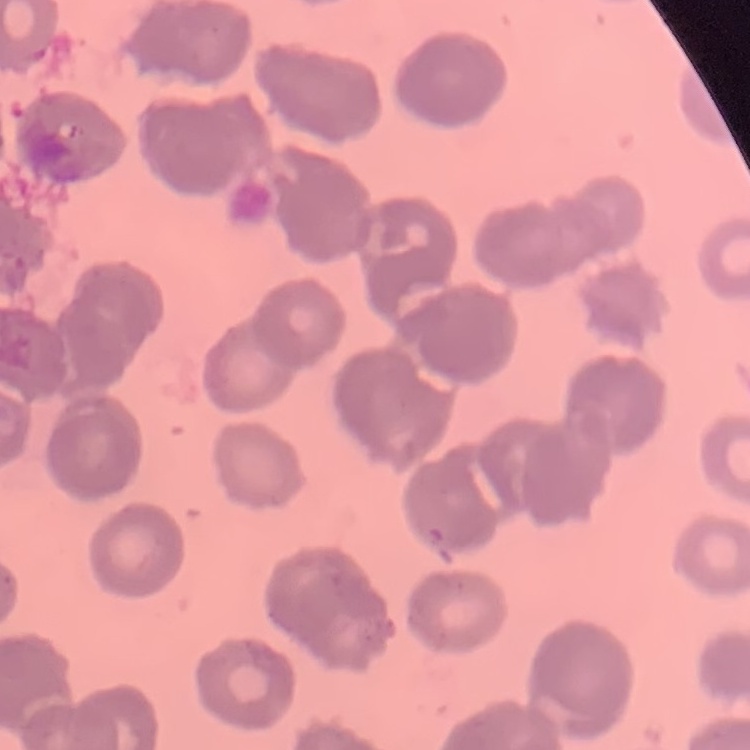
The red blood cells show rouleaux formation. Square crop of a larger photomicrograph. Thin blood smear. Stained with either Field's or Giemsa.